Evaluate for parasitized red blood cells.
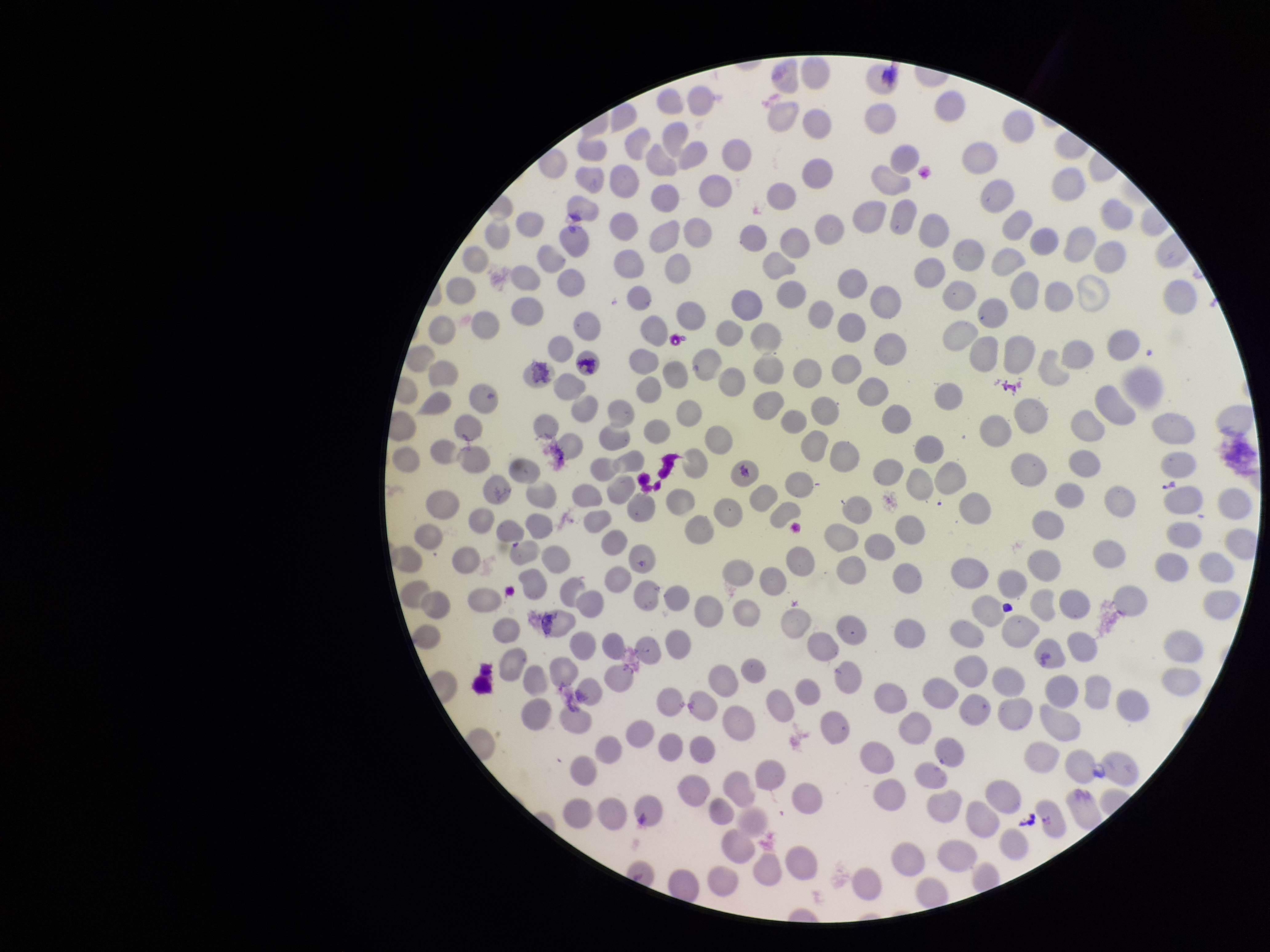

None seen.

Summary:
  - Field of view: single
  - Stain: Giemsa
  - Image size: 1270×952 pixels
  - Capture: smartphone photograph through the microscope eyepiece
  - Parasitized red blood cell count: 0
  - Preparation: thin blood smear
  - Red blood cell count: 290
  - Patient malaria status: negative